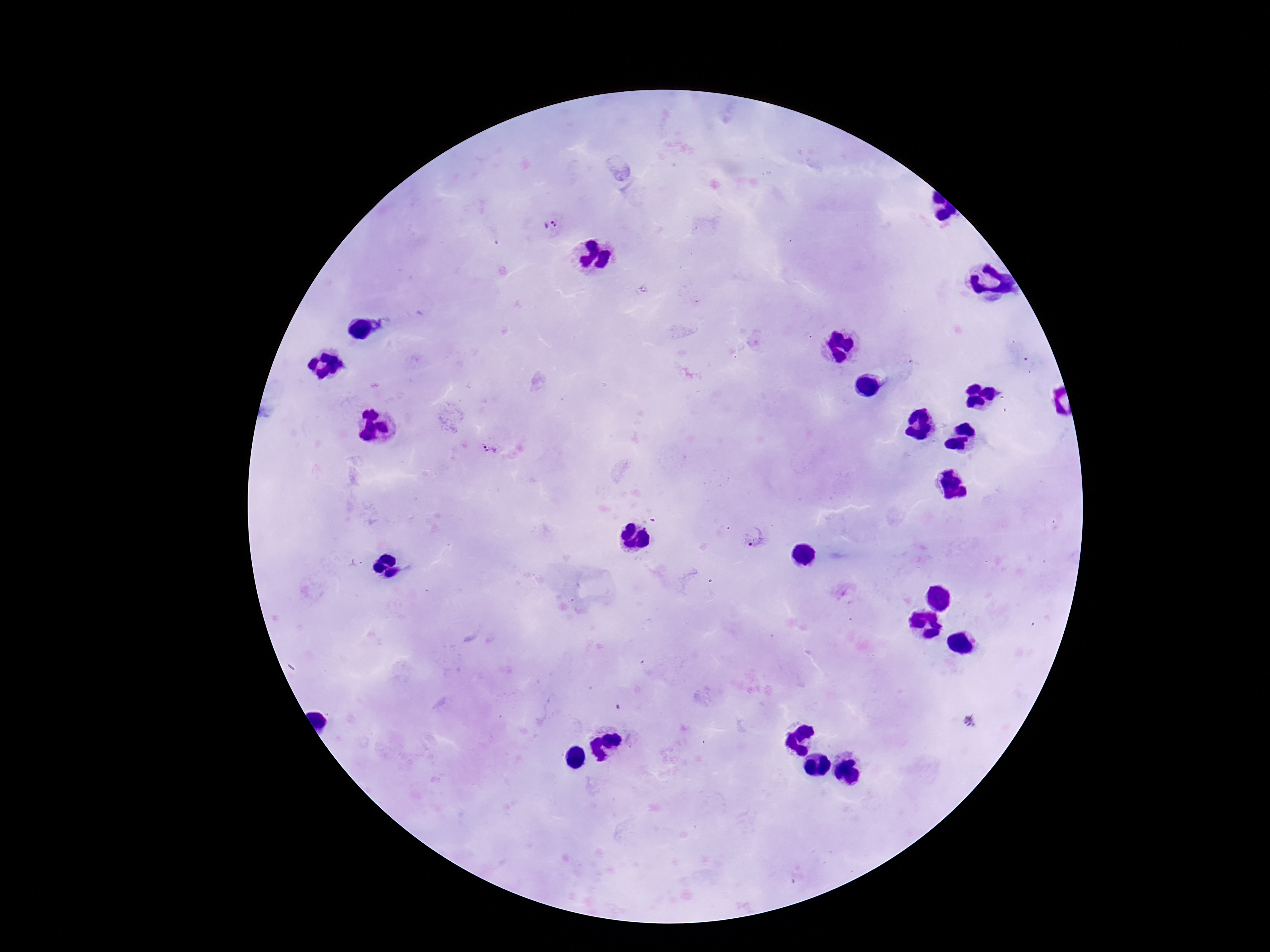

Approximate object centers, in pixels from the top-left corner.
Summary:
  - Plasmodium parasite locations: (x=549, y=226), (x=490, y=448), (x=753, y=536)
  - Patient malaria status: positive
  - Stain: Giemsa
  - Magnification: 100x
  - Image size: 1270×952 pixels
  - Field of view: single
  - Capture: smartphone camera through the microscope eyepiece
  - Preparation: thick blood smear